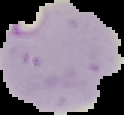

preparation: thin blood film
image_size: 124×115 pixels
malaria_status: parasitized
image_type: cell region segmented out of the field of view; surrounding area masked to black